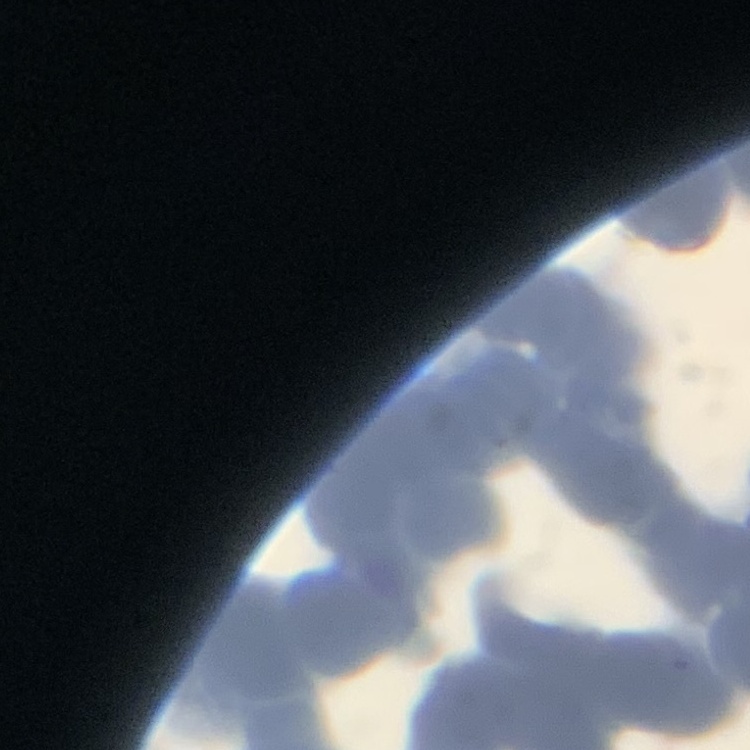

Summary:
  - Red blood cell morphology: rouleaux formation
  - Stain: Field's or Giemsa
  - Preparation: thin blood smear
  - Image type: one tile cut from a larger photomicrograph